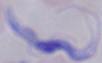
modality = micrograph
magnification = 1000x
identification = trypanosome